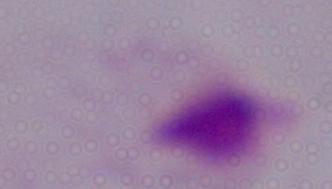

identification: trichomonad
modality: photomicrograph
magnification: 1000x